Name the parasite shown.
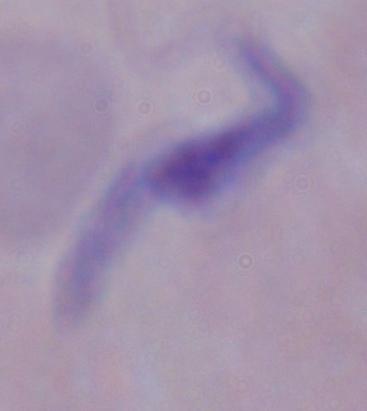
This is a trypanosome.

magnification = 1000x
modality = photomicrograph